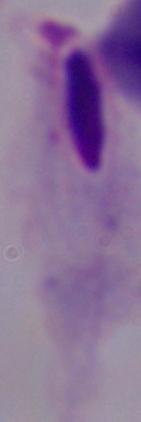

identification = trichomonad
modality = photomicrograph
magnification = 1000x